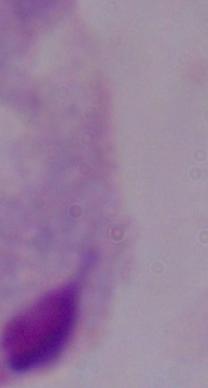

Summary:
  - Identification: trichomonad
  - Modality: photomicrograph
  - Magnification: 1000x